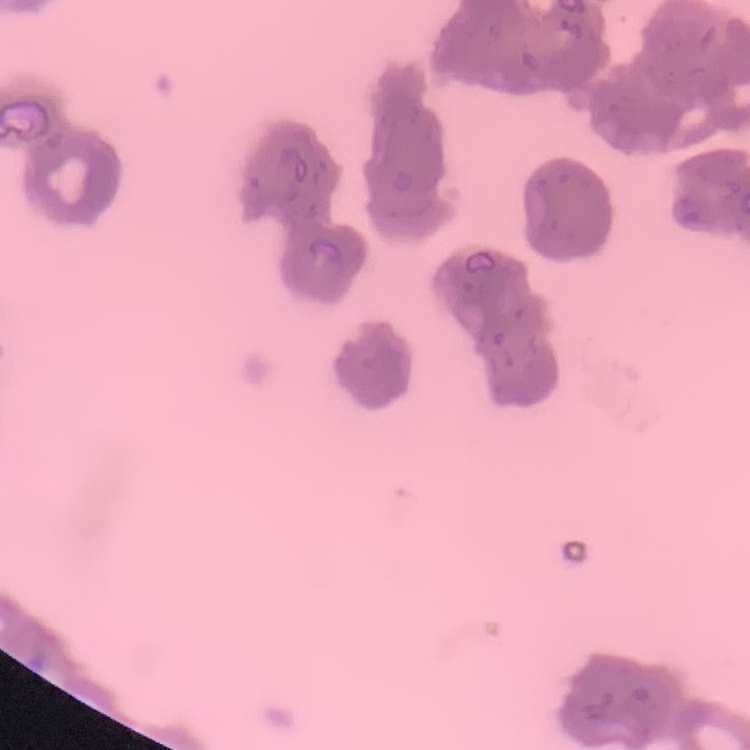

Summary:
  - Erythrocyte morphology: rouleaux formation
  - Preparation: thin peripheral smear
  - Image type: one tile cut from a larger photomicrograph
  - Stain: Field's or Giemsa